Classify this cell by malaria status.
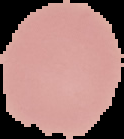
Uninfected.

image type = segmented cell region on a black background
preparation = thin blood smear
image size = 124×139 pixels